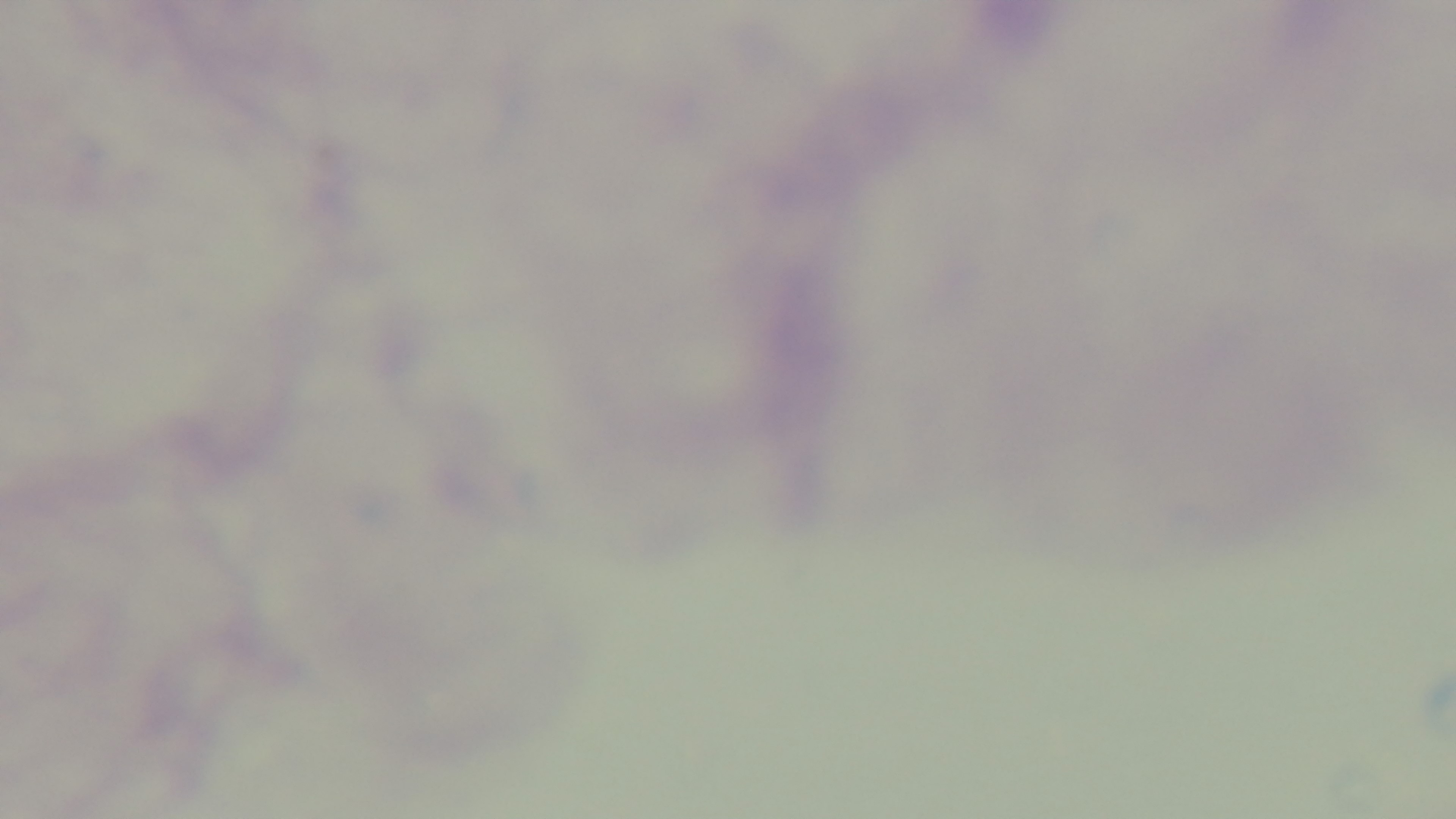

Summary:
  - Modality: light microscopy
  - Stain: Giemsa
  - Malaria status: uninfected
  - Preparation: thick blood film
  - Objective: 100x oil immersion
  - Capture: mounted 4K digital camera
  - Field of view: one from the slide